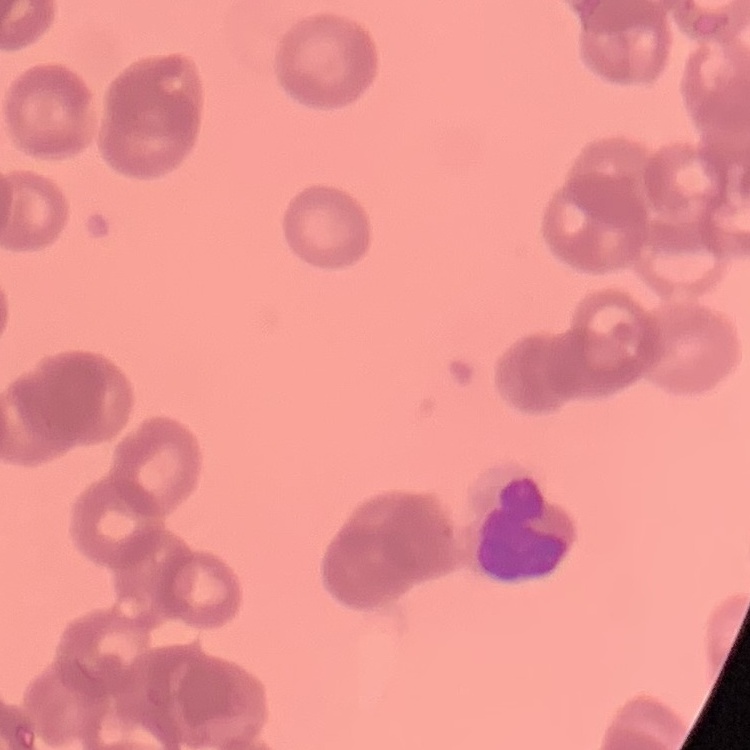
erythrocyte morphology = rouleaux formation
stain = Field's or Giemsa
preparation = thin blood smear
image type = one tile cut from a larger photomicrograph